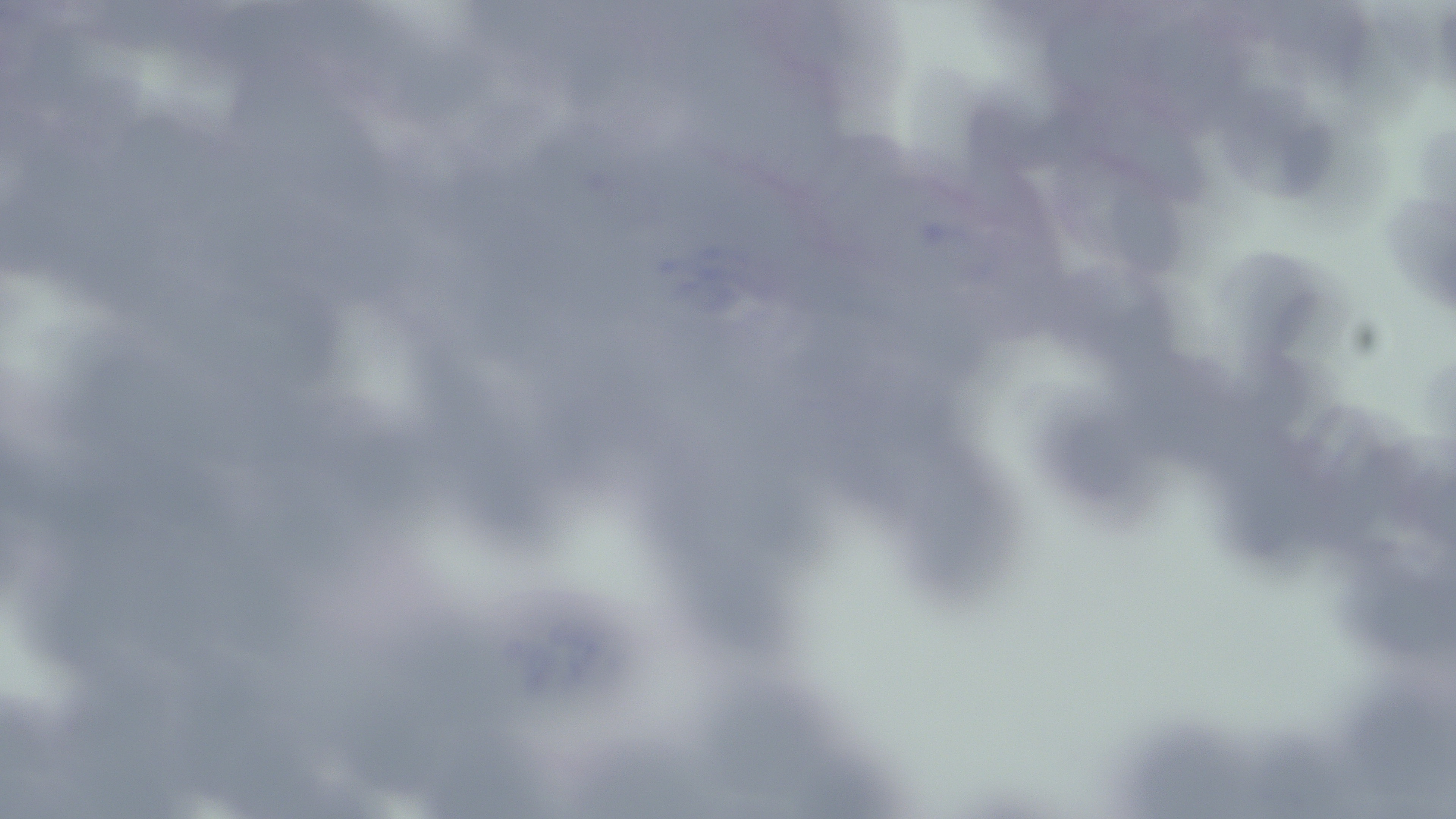
Approximate bounding boxes as (x1,y1)-(x2,y2) corner pairs in pixels. Uninfected red blood cell locations: (216,54)-(389,200), (678,55)-(850,196), (1225,82)-(1342,204), (1081,89)-(1216,211), (115,120)-(249,230), (383,124)-(536,238), (818,132)-(926,266), (1054,163)-(1203,273), (1384,191)-(1456,309), (956,222)-(1071,357), (1225,244)-(1357,376), (1054,267)-(1203,381), (220,269)-(353,397), (86,341)-(213,466), (1133,349)-(1278,470), (422,353)-(567,545), (1031,392)-(1164,540), (1208,430)-(1335,584), (906,447)-(1022,604), (650,488)-(807,663), (1350,530)-(1456,655), (174,664)-(312,798), (702,667)-(854,805), (1342,675)-(1453,817), (1118,713)-(1268,819), (420,718)-(572,819), (555,735)-(720,819), (235,753)-(401,817). Slide-level diagnosis: Babesia divergens. Optical microscopy. Thin blood smear. Single field of view. May-Grünwald-Giemsa-stained preparation. Captured at 1000x magnification. Image is 1456×819 pixels.